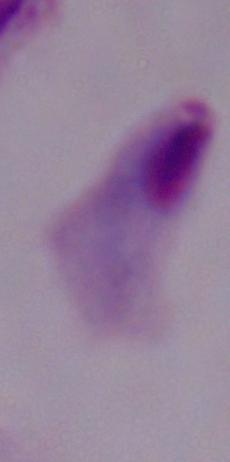

Captured at 1000x magnification. Photomicrograph. A trichomonad is seen.